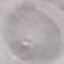

Summary:
  - Result: no malaria parasites detected
  - Stain: Giemsa
  - Image type: cell patch, automatically extracted from a larger field of view and resized to 64 × 64 pixels
  - Preparation: thin blood film
  - Capture: smartphone camera at the microscope eyepiece